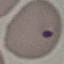
Result: malaria parasites identified. Thin blood film. Cell patch, automatically extracted from a larger field of view and resized to 64 × 64 pixels. Giemsa-stained preparation. Photographed with a smartphone camera at the microscope eyepiece.